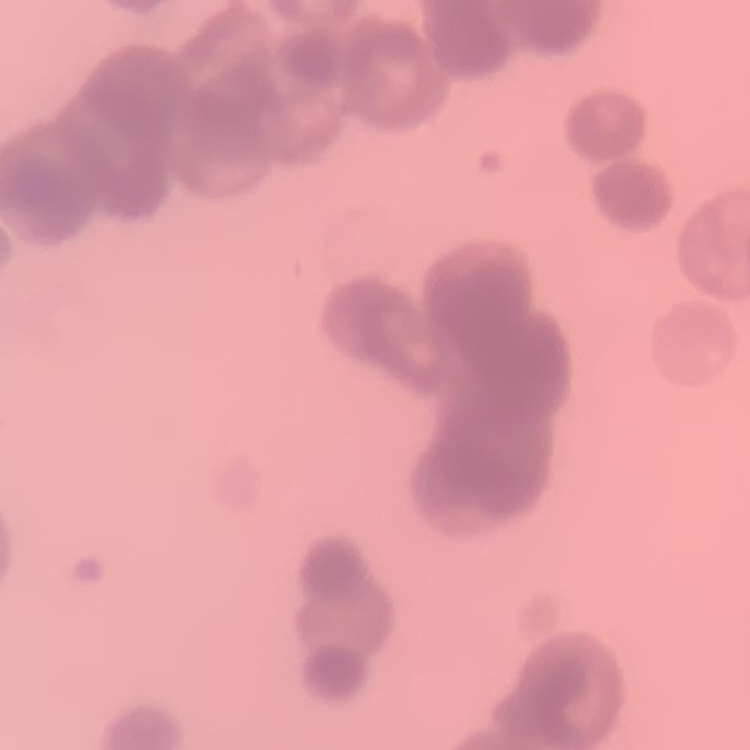
The erythrocytes exhibit rouleaux formation. Stained with either Field's or Giemsa. Thin blood smear. Square crop of a larger photomicrograph.